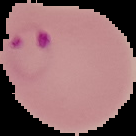
Summary:
  - Image type: segmented cell region with the area outside set to black
  - Preparation: thin blood film
  - Image size: 136×136 pixels
  - Malaria status: parasitized